Locate and identify every blood parasite.
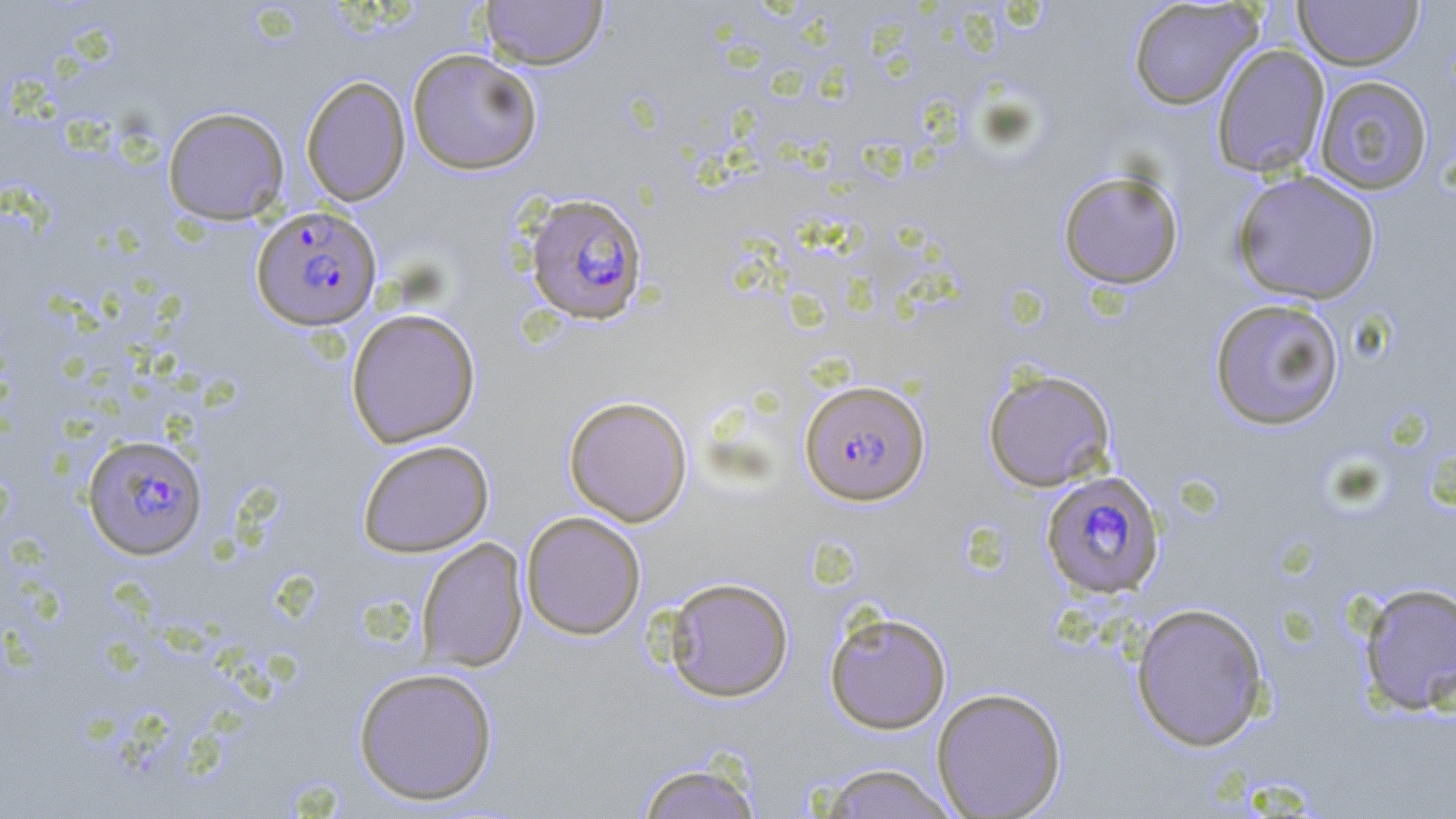

Approximate bounding boxes as (x1, y1, x2, y2) in pixels.
Plasmodium falciparum-infected red blood cells (subset): (251, 205, 381, 330), (799, 378, 931, 506), (82, 433, 208, 559), (1040, 470, 1165, 599).
No Plasmodium ovale, Plasmodium malariae, Plasmodium vivax, Babesia divergens, or Trypanosoma brucei observed.

Uninfected red blood cell locations (subset): (1127, 0, 1263, 111), (1294, 0, 1424, 71), (480, 1, 608, 70), (1210, 44, 1330, 178), (406, 48, 542, 175), (1314, 75, 1433, 195), (301, 76, 411, 206), (162, 106, 290, 225), (1057, 170, 1185, 289), (1230, 170, 1382, 305), (1208, 298, 1345, 431), (345, 308, 481, 448), (982, 367, 1117, 493), (563, 395, 693, 526), (357, 439, 494, 557), (521, 511, 646, 640), (416, 537, 529, 672), (664, 576, 794, 702), (1357, 581, 1456, 717), (1130, 601, 1270, 751), (824, 609, 952, 733), (353, 666, 499, 805), (931, 687, 1067, 818), (634, 761, 765, 819), (814, 762, 960, 819). Slide-level diagnosis: Plasmodium falciparum. May-Grünwald-Giemsa stain. Captured at 1000x magnification. Thin blood smear. Light microscopy. One field of a larger specimen. Image is 1456×819 pixels.